Classify this cell by malaria status.
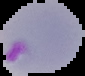
Parasitized.

From a thin blood film. Image is 85×76 pixels. The area outside the segmented cell region is set to black.